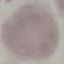

result: no malaria parasites seen
image_type: automatically extracted cell patch, resized to 64 × 64 pixels
capture: smartphone camera at the microscope eyepiece
preparation: thin blood film
stain: Giemsa